Describe the morphology of the erythrocytes.
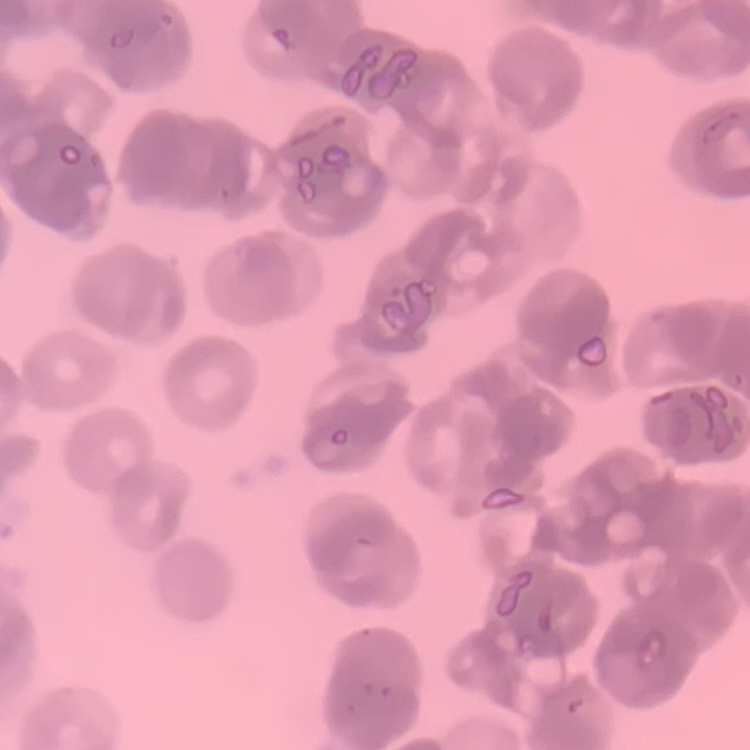
They show rouleaux formation.

Thin blood smear. Stained with either Field's or Giemsa. Square crop of a larger photomicrograph.